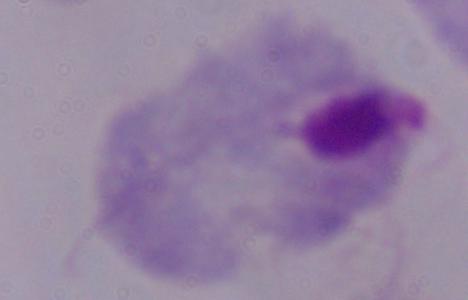 A trichomonad is seen. Micrograph. 1000x magnification.